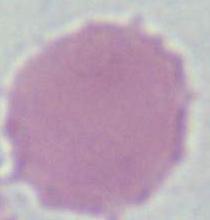

Micrograph. Captured at 1000x magnification. A red blood cell is seen.